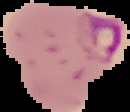
Image is 130×112 pixels. Result: malaria parasites identified. From a thin blood film. The area outside the segmented cell region is set to black.